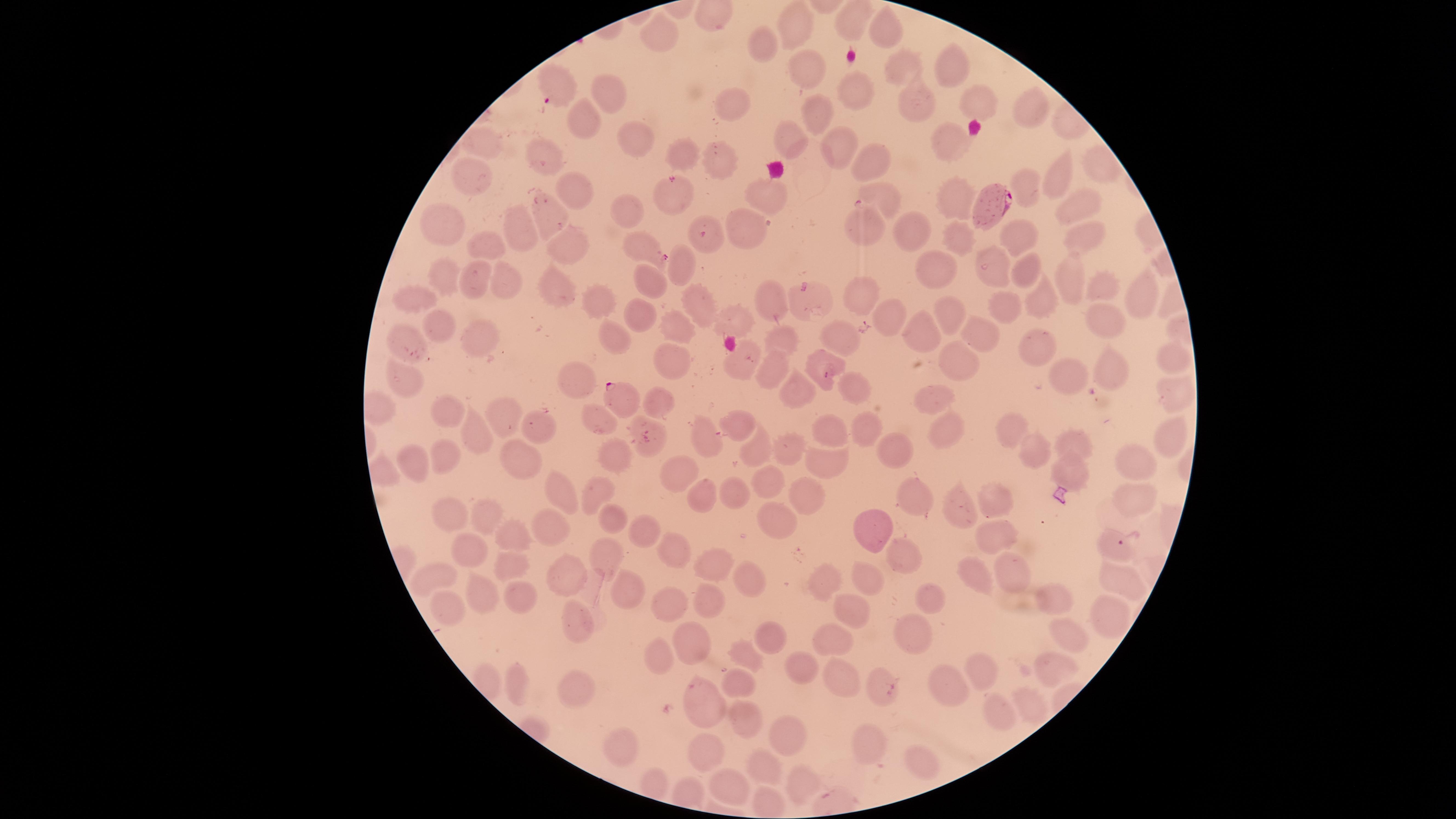

{
  "stain": "Giemsa",
  "species": "Plasmodium falciparum",
  "visible_region": "circular",
  "capture": "smartphone photograph through the microscope eyepiece",
  "image_size": "1456×819 pixels",
  "preparation": "thin blood film",
  "field_of_view": "single",
  "uninfected_red_blood_cells": "approximate marker points as {x, y} in pixels: {800, 25}, {882, 33}, {882, 34}, {663, 35}, {764, 41}, {950, 59}, {900, 66}, {805, 68}, {612, 87}, {857, 89}, {914, 97}, {737, 103}, {983, 110}, {1034, 111}, {812, 112}, {584, 120}, {627, 135}, {791, 137}, {953, 138}, {837, 142}, {481, 146}, {543, 152}, {678, 152}, {723, 157}, {869, 161}, {1059, 173}, {1029, 182}, {471, 184}, {576, 188}, {675, 191}, {771, 191}, {885, 195}, {958, 198}, {1078, 203}, {630, 205}, {550, 211}, {749, 223}, {866, 224}, {448, 226}, {519, 230}, {917, 232}, {1022, 235}, {1078, 235}, {960, 239}, {487, 241}, {640, 241}, {709, 241}, {570, 245}, {935, 265}, {679, 266}, {989, 266}, {1029, 272}, {445, 273}, {475, 276}, {510, 278}, {1067, 278}, {653, 280}, {1102, 282}, {550, 290}, {865, 291}, {589, 295}, {1139, 295}, {773, 297}, {411, 299}, {694, 301}, {1003, 304}, {1038, 308}, {637, 312}, {888, 314}, {947, 314}, {740, 316}, {1106, 320}, {678, 327}, {439, 328}, {980, 329}, {925, 331}, {616, 332}, {473, 333}, {844, 334}, {408, 337}, {781, 339}, {1036, 347}, {673, 355}, {961, 359}, {1170, 360}, {820, 363}, {742, 365}, {1116, 367}, {1064, 368}, {774, 369}, {406, 376}, {579, 382}, {852, 389}, {802, 391}, {1175, 391}, {934, 396}, {656, 403}, {446, 411}, {600, 417}, {741, 420}, {504, 421}, {1012, 422}, {543, 424}, {867, 428}, {705, 430}, {833, 431}, {951, 432}, {477, 433}, {1168, 436}, {1072, 441}, {893, 450}, {1035, 451}, {446, 452}, {757, 452}, {788, 453}, {616, 454}, {517, 458}, {1132, 460}, {412, 462}, {682, 465}, {823, 466}, {1069, 469}, {767, 479}, {558, 488}, {598, 491}, {728, 494}, {700, 496}, {801, 499}, {911, 499}, {1129, 499}, {999, 500}, {960, 506}, {456, 512}, {491, 517}, {777, 519}, {613, 523}, {869, 528}, {551, 531}, {646, 531}, {994, 532}, {511, 534}, {472, 546}, {674, 548}, {611, 555}, {508, 561}, {903, 561}, {712, 568}, {972, 571}, {878, 572}, {574, 575}, {437, 576}, {749, 576}, {1013, 576}, {1120, 578}, {828, 581}, {628, 588}, {478, 593}, {522, 595}, {1056, 595}, {708, 600}, {935, 600}, {451, 602}, {673, 606}, {853, 613}, {1105, 616}, {580, 624}, {910, 630}, {835, 634}, {771, 636}, {690, 637}, {1062, 640}, {657, 654}, {744, 656}, {798, 660}, {983, 665}, {1046, 670}, {839, 678}, {883, 684}, {943, 684}, {516, 685}, {738, 686}, {570, 693}, {703, 696}, {1027, 699}, {1000, 714}, {744, 716}, {789, 738}, {624, 741}, {873, 744}, {710, 752}, {912, 757}, {767, 767}, {803, 781}, {732, 790}",
  "presence": "malaria parasites detected",
  "parasitized_red_blood_cells": "approximate marker points as {x, y} in pixels: {554, 90}, {991, 204}, {622, 398}, {1111, 546}"
}